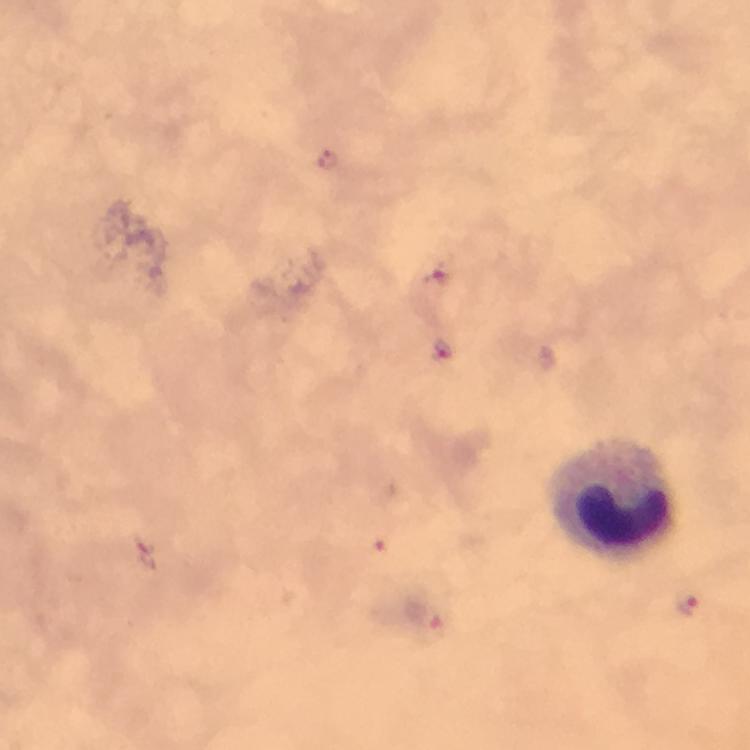
Approximate centers as {x, y} in pixels.
Summary:
  - Leukocyte locations: {611, 498}
  - Malaria parasite locations: {330, 160}, {435, 274}, {444, 355}, {374, 543}, {689, 606}, {425, 618}
  - Immersion oil: applied
  - Context: from a malaria diagnostic workup
  - Image size: 750×750 pixels
  - Stain: Giemsa
  - Capture: smartphone photograph through a microscope
  - Preparation: thick blood smear
  - Magnification: 100x
  - Cropped from: a single field of view